Give the position of every Plasmodium parasite visible.
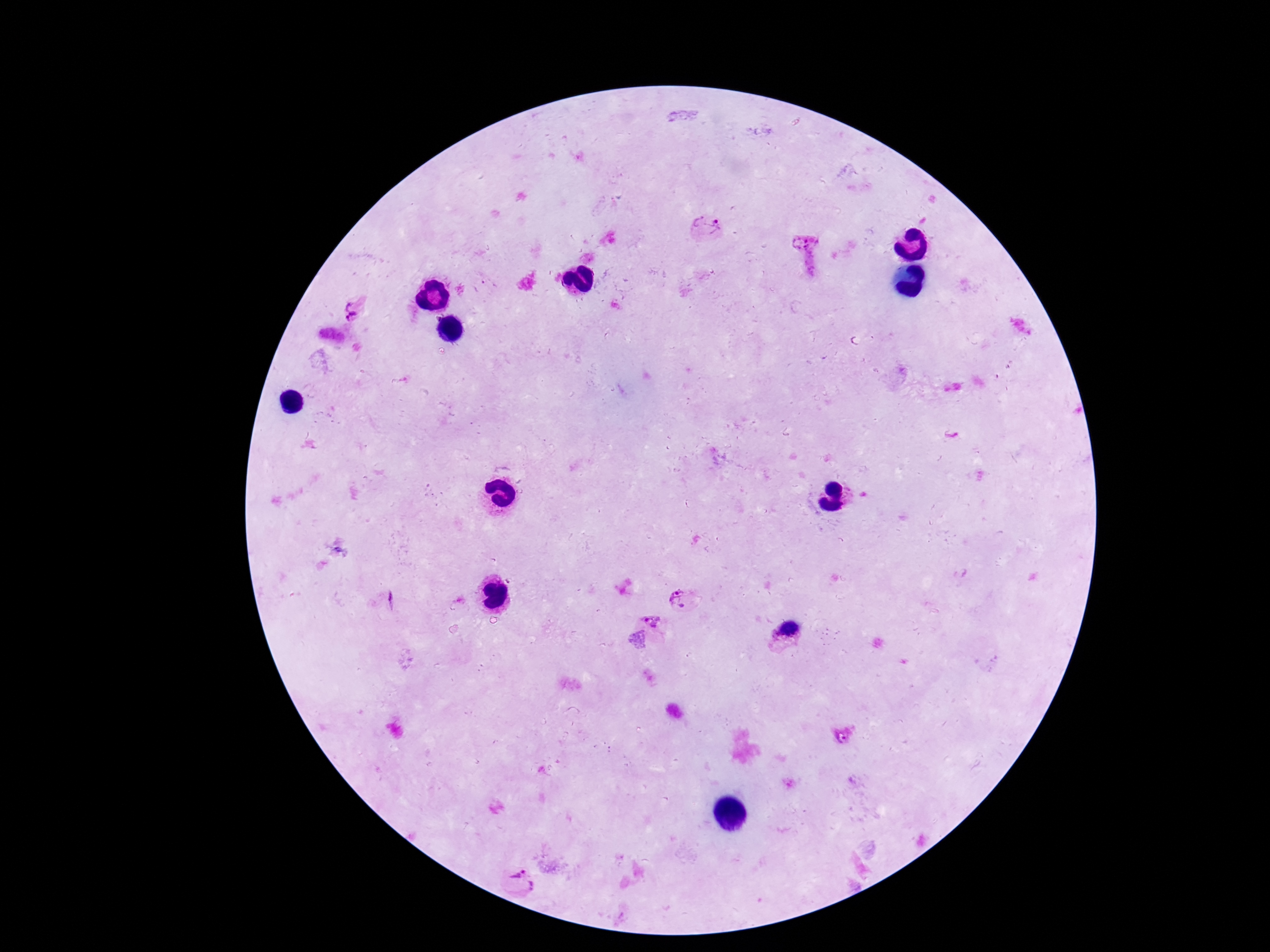
Approximate object centers, in pixels from the top-left corner.
Plasmodium parasites: (x=697, y=222), (x=712, y=227), (x=356, y=308), (x=680, y=598), (x=650, y=620), (x=788, y=627), (x=839, y=737), (x=521, y=882).

capture = smartphone camera through the microscope eyepiece
image size = 1270×952 pixels
magnification = 100x
field of view = single
stain = Giemsa
preparation = thick blood film
patient malaria status = positive